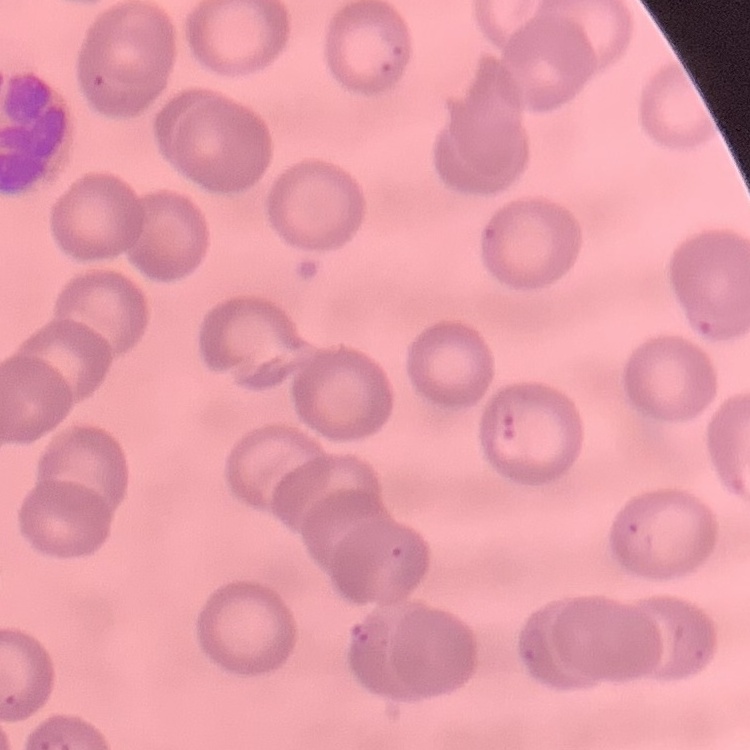
Summary:
  - Erythrocyte morphology: no rouleaux formation
  - Image type: square crop of a larger photomicrograph
  - Preparation: thin peripheral smear
  - Stain: Field's or Giemsa